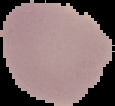

{
  "malaria_status": "uninfected",
  "image_size": "115×106 pixels",
  "preparation": "thin blood film",
  "image_type": "cell region segmented out of the field of view; surrounding area masked to black"
}